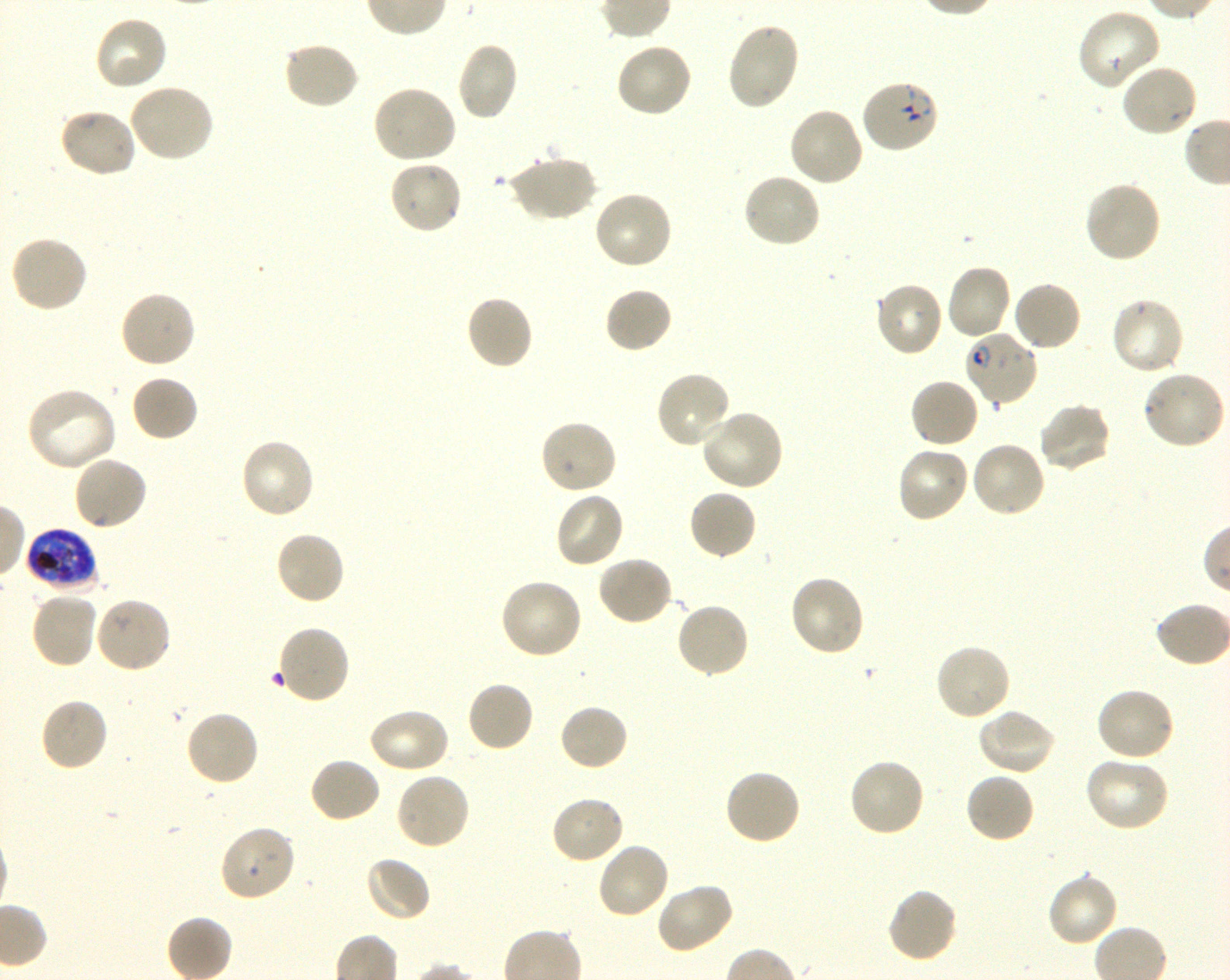 Approximate bounding boxes as [x1, y1, x2, y2] in pixels. Not every red blood cell is marked. A life-cycle stage — or a range of stages, where the recorded stages span more than one — follows each staged infected red blood cell. Locations of uninfected red blood cells: [1076, 8, 1163, 91], [93, 15, 169, 93], [725, 21, 801, 111], [282, 40, 360, 111], [456, 42, 520, 122], [615, 42, 692, 118], [1120, 63, 1200, 139], [128, 82, 215, 162], [371, 84, 458, 164], [788, 106, 865, 188], [57, 107, 138, 178], [505, 155, 596, 223], [388, 160, 464, 236], [741, 171, 823, 249], [1082, 179, 1162, 264], [592, 189, 674, 271], [9, 234, 89, 314], [945, 262, 1013, 339], [874, 280, 944, 358], [1011, 280, 1082, 352], [604, 286, 673, 354], [118, 289, 197, 369], [464, 294, 534, 372], [1110, 297, 1186, 377], [654, 369, 733, 450], [1139, 370, 1225, 451], [130, 373, 199, 443], [909, 378, 981, 449], [26, 385, 118, 473], [1037, 401, 1114, 473], [699, 409, 784, 493], [538, 418, 618, 495], [239, 437, 317, 520], [969, 440, 1046, 519], [896, 445, 971, 524], [72, 455, 149, 532], [687, 488, 758, 561], [553, 491, 625, 570], [274, 530, 346, 607], [596, 554, 674, 627], [788, 574, 867, 657], [499, 577, 584, 661], [30, 591, 98, 670], [93, 596, 172, 674], [675, 601, 750, 679], [934, 642, 1013, 722], [465, 680, 535, 753], [1094, 686, 1177, 763], [38, 696, 110, 772], [558, 703, 630, 772], [366, 706, 451, 776], [975, 708, 1056, 777], [185, 710, 260, 787], [309, 756, 382, 824], [1083, 756, 1170, 833], [847, 757, 926, 838], [722, 769, 802, 846], [394, 771, 472, 850], [964, 772, 1036, 845], [550, 794, 626, 865], [218, 824, 297, 903], [595, 841, 671, 921], [363, 855, 431, 923], [1046, 871, 1120, 947], [654, 881, 735, 955], [885, 886, 959, 964]. Locations of red blood cells of indeterminate infection status: [275, 624, 351, 706]. Locations of infected red blood cells: [859, 78, 941, 155] early ring to early trophozoite; [962, 329, 1039, 406] early ring to early trophozoite; [25, 527, 100, 592] late trophozoite to late schizont. Giemsa stain. Image is 1230×980 pixels. One field from this slide. Plasmodium falciparum strain 3D7 in shaking in-vitro culture. 100x objective under oil immersion, numerical aperture 1.30. Thin blood smear. Donor blood group O+.